State which cell type is depicted.
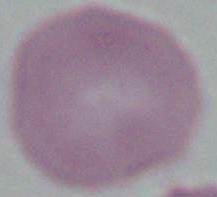
An erythrocyte.

Micrograph. 1000x magnification.